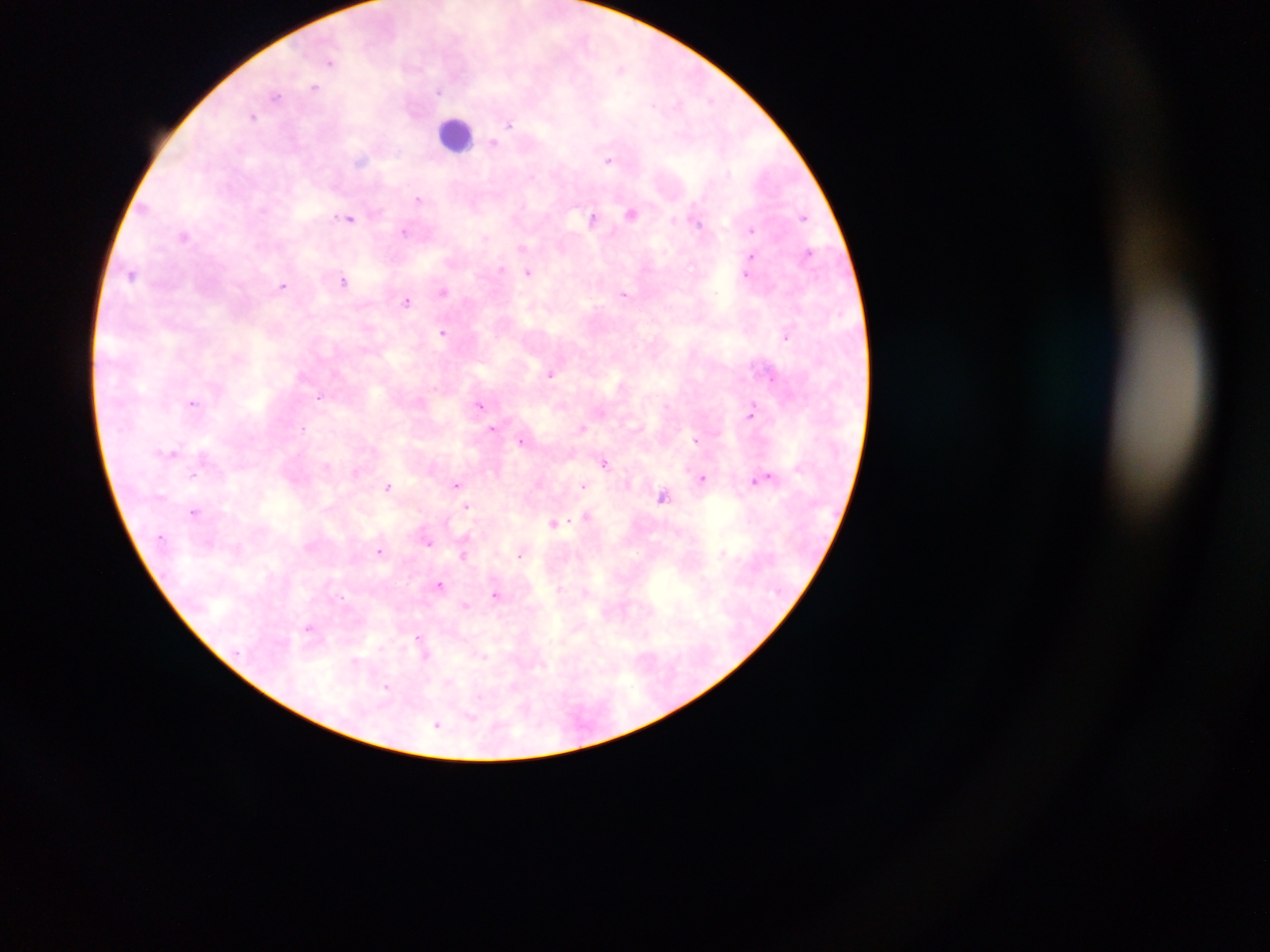

capture: mobile-phone photograph through a microscope
leukocyte_locations: 'approximate centers as [x, y] in pixels: [456, 134]'
malaria_parasite_locations: 'approximate centers as [x, y] in pixels: [330, 62], [315, 87], [438, 92], [275, 95], [253, 116], [509, 124], [493, 142], [609, 159], [362, 160], [729, 173], [419, 198], [144, 208], [631, 214], [804, 217], [350, 218], [594, 218], [674, 219], [696, 220], [751, 229], [404, 231], [184, 236], [522, 248], [808, 252], [751, 256], [501, 269], [133, 273], [528, 273], [747, 275], [344, 281], [283, 286], [443, 291], [623, 294], [406, 301], [443, 332], [786, 336], [551, 374], [771, 378], [320, 396], [192, 403], [479, 405], [751, 412], [303, 427], [492, 428], [582, 428], [696, 440], [521, 441], [173, 452], [604, 463], [327, 465], [356, 473], [193, 475], [703, 478], [764, 478], [456, 484], [583, 486], [388, 487], [662, 496], [467, 506], [195, 512], [586, 517], [553, 523], [428, 542], [380, 550], [722, 553], [463, 554], [521, 554], [440, 585], [495, 594], [466, 605], [308, 628], [419, 638], [423, 647], [381, 648], [425, 654], [483, 656], [355, 661], [387, 688], [471, 715], [437, 724]'
image_size: 1270×952 pixels
preparation: thick blood film
country: Ghana
field_of_view: single